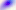
modality: micrograph
identification: Toxoplasma gondii
magnification: 400x